Outline each Plasmodium ovale-infected red blood cell.
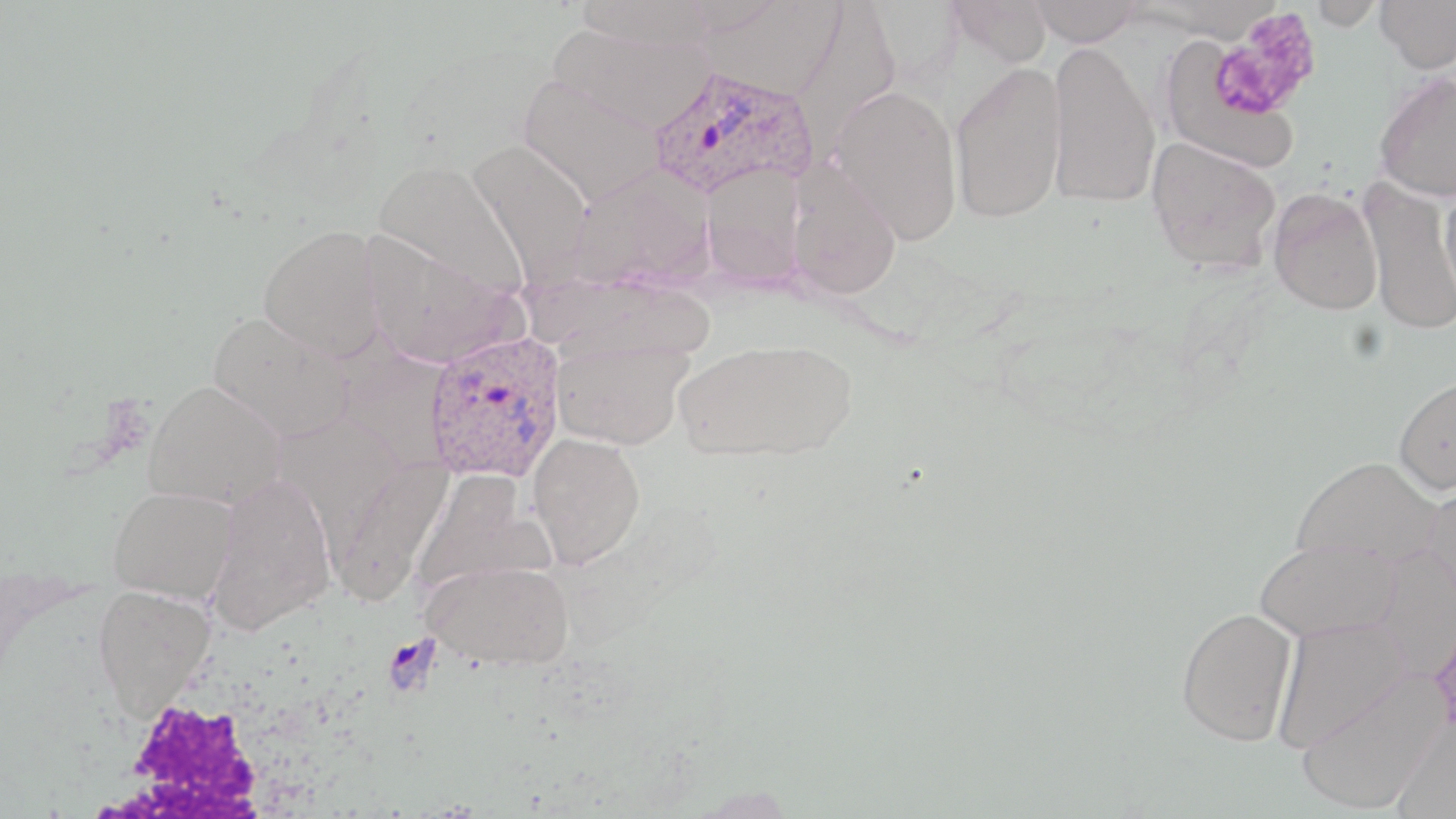
Approximate bounding boxes as named x1/y1/x2/y2 corners in pixels.
Plasmodium ovale-infected red blood cells: (x1=649, y1=65, x2=819, y2=200), (x1=423, y1=330, x2=567, y2=483).

slide-level diagnosis = Plasmodium ovale
modality = optical microscopy
magnification = 1000x
stain = May-Grünwald-Giemsa
platelet locations = approximate bounding boxes as named x1/y1/x2/y2 corners in pixels: (x1=1211, y1=11, x2=1322, y2=120)
preparation = thin blood film
white blood cell locations = approximate bounding boxes as named x1/y1/x2/y2 corners in pixels: (x1=86, y1=682, x2=298, y2=819)
uninfected red blood cell locations = approximate bounding boxes as named x1/y1/x2/y2 corners in pixels: (x1=575, y1=0, x2=716, y2=51), (x1=946, y1=0, x2=1052, y2=68), (x1=1030, y1=0, x2=1144, y2=46), (x1=1307, y1=0, x2=1387, y2=30), (x1=1375, y1=0, x2=1456, y2=73), (x1=702, y1=1, x2=848, y2=101), (x1=787, y1=5, x2=900, y2=150), (x1=548, y1=22, x2=716, y2=136), (x1=1047, y1=41, x2=1161, y2=210), (x1=1160, y1=41, x2=1297, y2=170), (x1=949, y1=62, x2=1066, y2=224), (x1=1373, y1=71, x2=1456, y2=202), (x1=516, y1=74, x2=666, y2=206), (x1=831, y1=83, x2=964, y2=245), (x1=1146, y1=137, x2=1281, y2=272), (x1=468, y1=140, x2=593, y2=286), (x1=372, y1=160, x2=529, y2=299), (x1=700, y1=161, x2=808, y2=287), (x1=788, y1=162, x2=902, y2=300), (x1=568, y1=166, x2=716, y2=291), (x1=1438, y1=176, x2=1456, y2=303), (x1=1362, y1=180, x2=1456, y2=335), (x1=1268, y1=189, x2=1382, y2=315), (x1=259, y1=223, x2=386, y2=360), (x1=362, y1=231, x2=523, y2=369), (x1=208, y1=311, x2=354, y2=445), (x1=552, y1=338, x2=693, y2=450), (x1=675, y1=338, x2=858, y2=462), (x1=1394, y1=374, x2=1456, y2=495), (x1=144, y1=380, x2=285, y2=507), (x1=527, y1=432, x2=646, y2=569), (x1=1291, y1=455, x2=1443, y2=569), (x1=326, y1=457, x2=452, y2=608), (x1=410, y1=472, x2=549, y2=599), (x1=207, y1=473, x2=336, y2=636), (x1=1422, y1=476, x2=1456, y2=610), (x1=108, y1=486, x2=239, y2=603), (x1=1254, y1=538, x2=1402, y2=642), (x1=1370, y1=546, x2=1456, y2=679), (x1=422, y1=559, x2=574, y2=670), (x1=92, y1=584, x2=216, y2=714), (x1=1176, y1=606, x2=1298, y2=746), (x1=1272, y1=617, x2=1410, y2=754), (x1=1295, y1=671, x2=1447, y2=814), (x1=1390, y1=713, x2=1456, y2=817)
field of view = single
image size = 1456×819 pixels